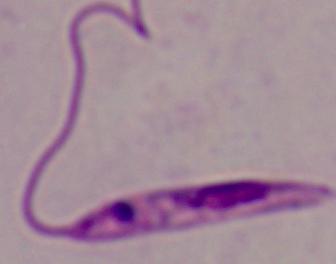

modality: photomicrograph
magnification: 1000x
identification: Leishmania